Describe the morphology of the erythrocytes.
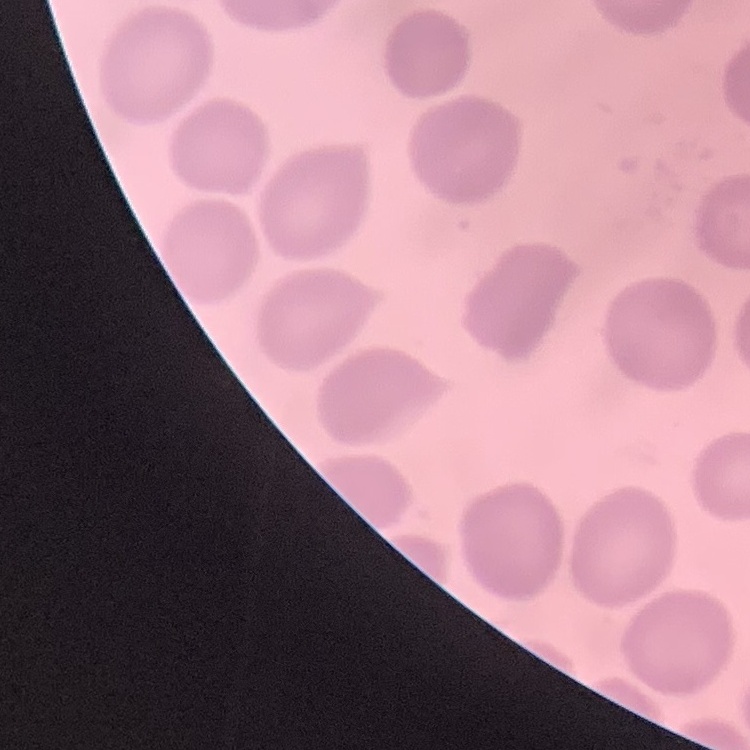

They show no rouleaux formation.

Summary:
  - Preparation: thin blood smear
  - Stain: Field's or Giemsa
  - Image type: square crop of a larger photomicrograph